Report the malaria status of this cell.
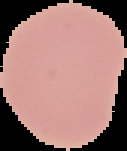
It is uninfected.

Segmented cell region on a black background. Image is 127×151 pixels. From a thin blood smear.